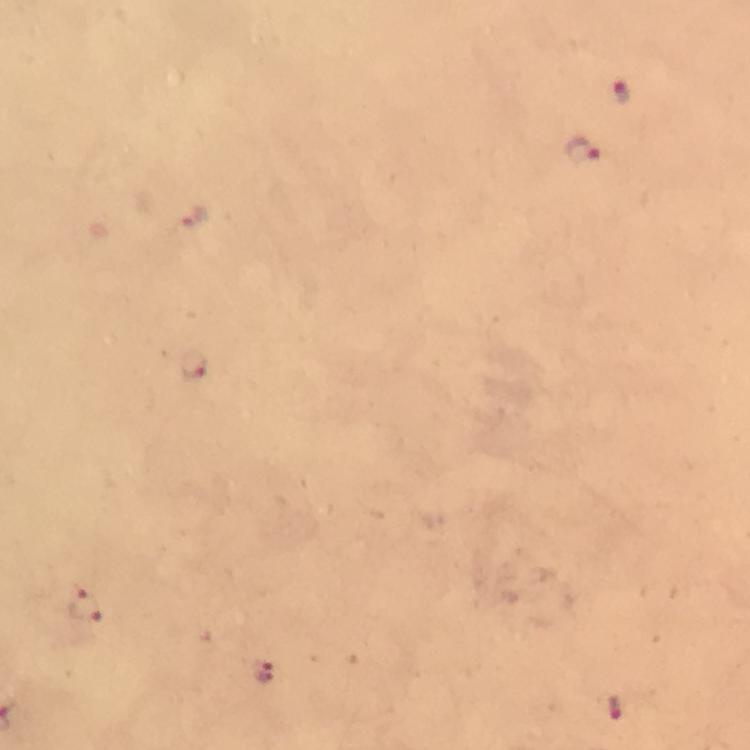
Approximate centers as {x, y} in pixels.
Summary:
  - Malaria parasite locations: {622, 90}, {583, 150}, {192, 218}, {194, 366}, {86, 607}, {262, 671}, {615, 706}
  - Immersion oil: used
  - Stain: Giemsa
  - Image size: 750×750 pixels
  - Capture: smartphone mounted on the microscope
  - Cropped from: one field of view
  - Preparation: thick blood film
  - Context: from a malaria diagnostic workup
  - Magnification: 100x